State which cell type is depicted.
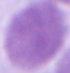

This is an erythrocyte.

magnification: 1000x
modality: micrograph